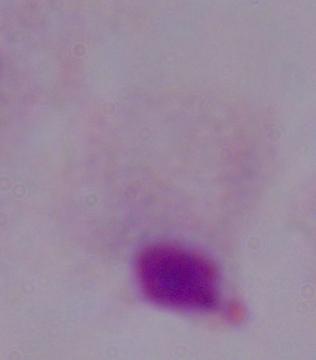
modality = micrograph
identification = trichomonad
magnification = 1000x